Look for Plasmodium parasites.
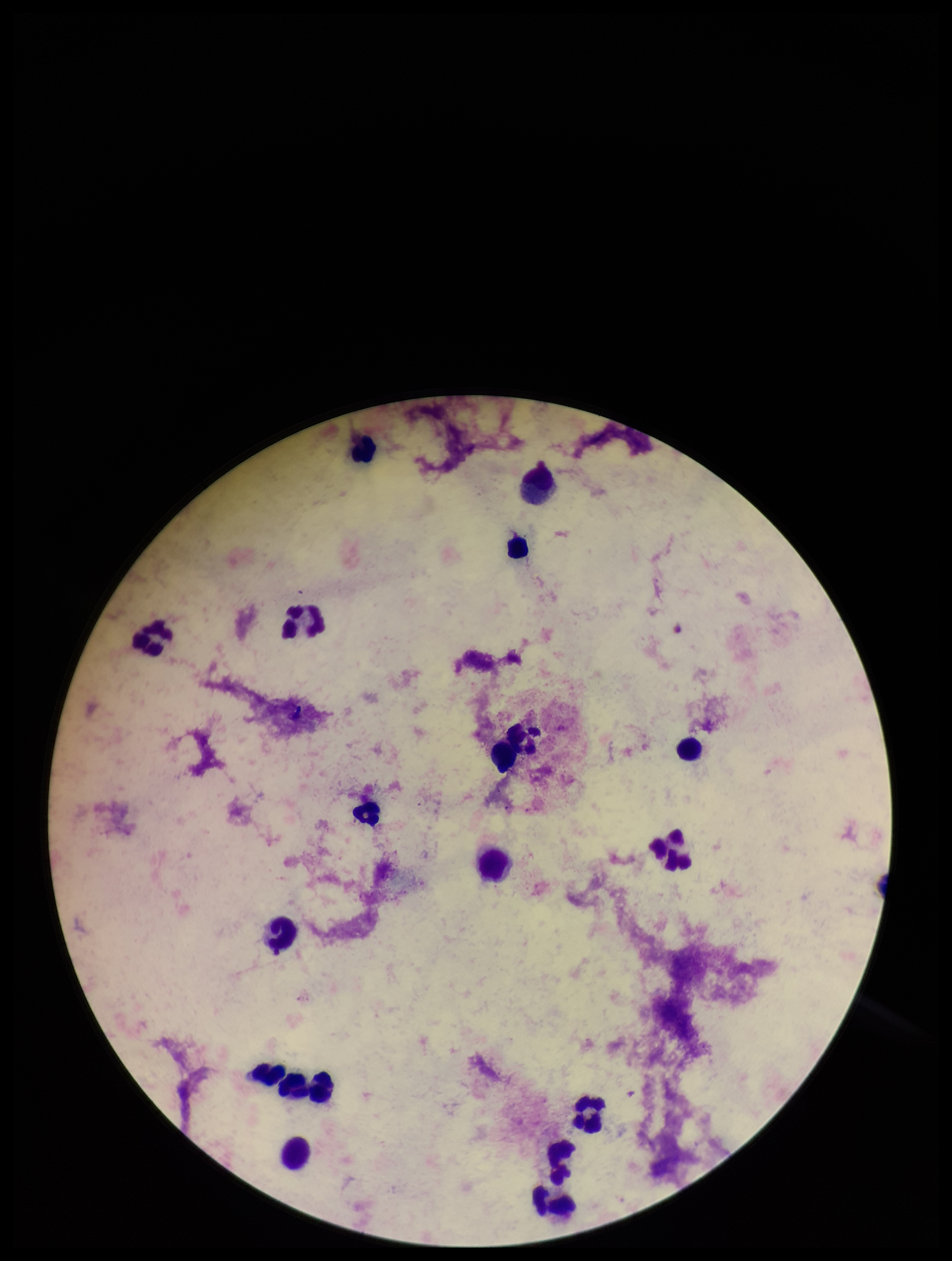

None detected.

Leukocyte count: 17. Smartphone photograph taken through the eyepiece of a microscope. Image is 952×1261 pixels. Stained with Giemsa. One field from this slide. Parasite count: 0. Preparation: thick smear. Patient malaria status: negative.